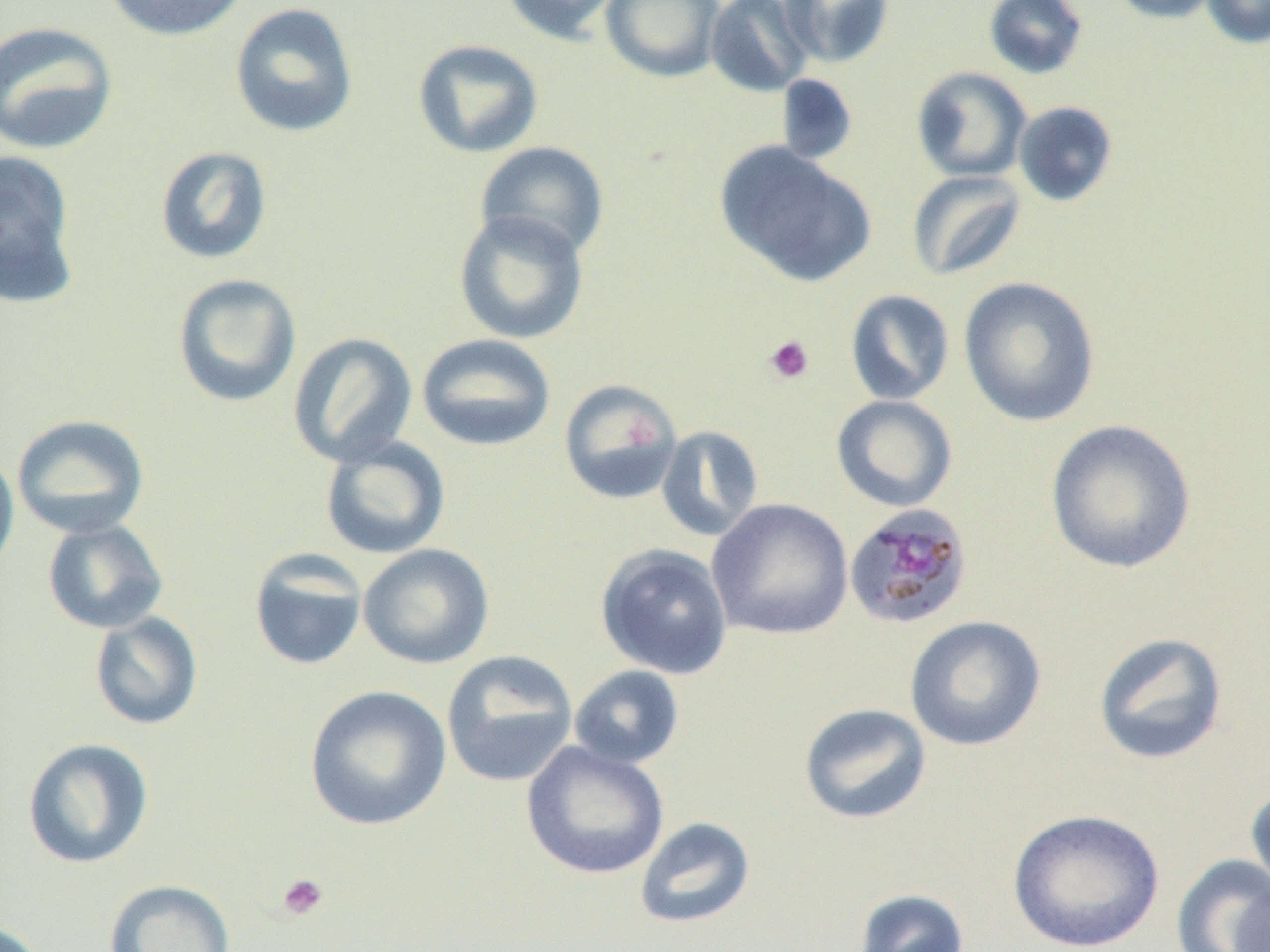

Summary:
  - Coordinate format: approximate bounding boxes as named x1/y1/x2/y2 corners in pixels
  - Uninfected red blood cell locations: (x1=103, y1=0, x2=251, y2=42), (x1=501, y1=0, x2=625, y2=45), (x1=600, y1=0, x2=727, y2=82), (x1=705, y1=0, x2=816, y2=98), (x1=780, y1=0, x2=894, y2=68), (x1=982, y1=0, x2=1089, y2=80), (x1=1107, y1=0, x2=1223, y2=24), (x1=1201, y1=0, x2=1270, y2=49), (x1=229, y1=2, x2=359, y2=138), (x1=0, y1=20, x2=118, y2=155), (x1=412, y1=39, x2=544, y2=158), (x1=911, y1=66, x2=1032, y2=183), (x1=776, y1=74, x2=859, y2=166), (x1=1013, y1=101, x2=1119, y2=207), (x1=474, y1=141, x2=610, y2=262), (x1=715, y1=141, x2=877, y2=288), (x1=155, y1=146, x2=273, y2=265), (x1=0, y1=148, x2=81, y2=306), (x1=907, y1=170, x2=1027, y2=281), (x1=452, y1=210, x2=591, y2=344), (x1=172, y1=273, x2=302, y2=408), (x1=957, y1=276, x2=1101, y2=427), (x1=845, y1=289, x2=955, y2=406), (x1=288, y1=332, x2=418, y2=467), (x1=416, y1=333, x2=556, y2=452), (x1=558, y1=378, x2=683, y2=505), (x1=831, y1=395, x2=958, y2=512), (x1=11, y1=414, x2=150, y2=538), (x1=1045, y1=419, x2=1197, y2=574), (x1=655, y1=425, x2=764, y2=542), (x1=319, y1=437, x2=451, y2=560), (x1=0, y1=446, x2=19, y2=581), (x1=707, y1=498, x2=854, y2=640), (x1=41, y1=518, x2=169, y2=634), (x1=358, y1=544, x2=494, y2=669), (x1=595, y1=544, x2=734, y2=679), (x1=249, y1=550, x2=369, y2=672), (x1=89, y1=612, x2=204, y2=731), (x1=904, y1=615, x2=1046, y2=752), (x1=1092, y1=631, x2=1229, y2=765), (x1=442, y1=650, x2=579, y2=788), (x1=569, y1=665, x2=685, y2=769), (x1=304, y1=684, x2=451, y2=831), (x1=798, y1=703, x2=932, y2=825), (x1=22, y1=737, x2=155, y2=869), (x1=521, y1=740, x2=669, y2=880), (x1=1245, y1=783, x2=1270, y2=901), (x1=1007, y1=808, x2=1165, y2=951), (x1=634, y1=816, x2=756, y2=930), (x1=1171, y1=854, x2=1270, y2=952), (x1=103, y1=879, x2=237, y2=952), (x1=853, y1=888, x2=970, y2=952), (x1=1229, y1=889, x2=1270, y2=952), (x1=0, y1=918, x2=48, y2=952)
  - Platelet locations: (x1=762, y1=334, x2=815, y2=385), (x1=276, y1=872, x2=329, y2=921)
  - Plasmodium malariae-infected red blood cell locations: (x1=843, y1=502, x2=974, y2=631)
  - Slide-level diagnosis: Plasmodium malariae
  - Preparation: thin blood smear
  - Image size: 1270×952 pixels
  - Magnification: 1000x
  - Modality: optical microscopy
  - Field of view: single